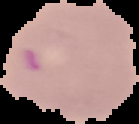
Summary:
  - Image type: segmented cell region on a black background
  - Malaria status: parasitized
  - Preparation: thin blood film
  - Image size: 139×124 pixels